Outline each blood parasite and name the species.
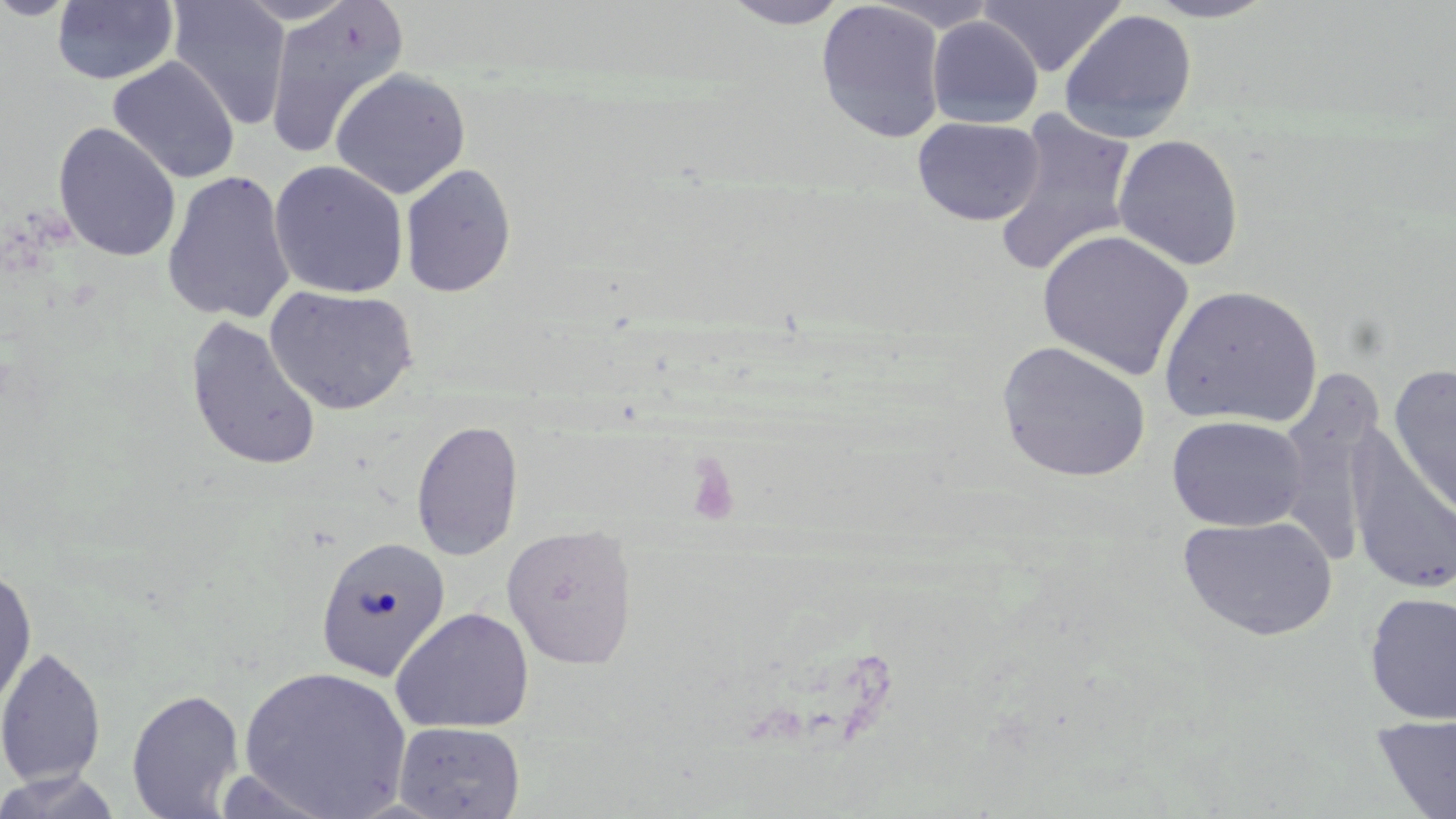

No blood parasites observed.

Approximate bounding boxes as [x1, y1, x2, y2] in pixels. Platelet locations: [683, 454, 741, 527]. Uninfected red blood cell locations: [0, 0, 83, 21], [167, 0, 292, 130], [263, 0, 409, 160], [718, 0, 852, 29], [865, 0, 1003, 31], [979, 0, 1127, 77], [1143, 0, 1278, 23], [51, 1, 179, 86], [815, 1, 947, 143], [1057, 8, 1198, 142], [926, 16, 1044, 128], [107, 56, 241, 185], [329, 68, 471, 199], [993, 110, 1139, 278], [912, 116, 1046, 226], [53, 122, 181, 262], [1113, 134, 1244, 271], [269, 160, 409, 300], [399, 163, 517, 298], [161, 169, 296, 326], [1037, 229, 1193, 380], [265, 285, 419, 415], [1159, 285, 1323, 430], [184, 315, 323, 473], [996, 341, 1152, 483], [1389, 364, 1456, 518], [1167, 414, 1310, 532], [411, 419, 524, 561], [1348, 430, 1456, 599], [1178, 514, 1339, 640], [501, 524, 639, 670], [315, 535, 452, 682], [0, 565, 37, 715], [1363, 591, 1456, 725], [390, 606, 535, 734], [0, 646, 106, 789], [238, 666, 413, 819], [126, 688, 245, 818], [1372, 714, 1456, 819], [394, 721, 526, 818], [0, 769, 125, 819]. Slide-level diagnosis: negative for blood parasites. Single field of view. Captured at 1000x magnification. Optical microscopy. May-Grünwald-Giemsa stain. Image is 1456×819 pixels. Thin blood film.